Assess this cell for malaria.
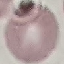

It is uninfected.

Automatically extracted cell patch, resized to 64 × 64 pixels. Thin blood film. Giemsa-stained preparation. Acquired by smartphone through the microscope eyepiece.